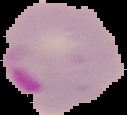
result = Plasmodium parasites detected
preparation = thin blood smear
image size = 127×115 pixels
image type = segmented cell region on a black background